Name the parasite shown.
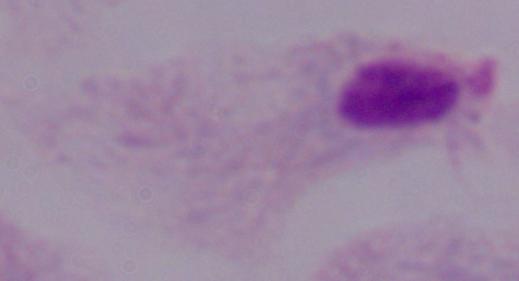

A trichomonad.

modality = micrograph
magnification = 1000x